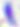 400x magnification. Photomicrograph. Toxoplasma gondii is seen.